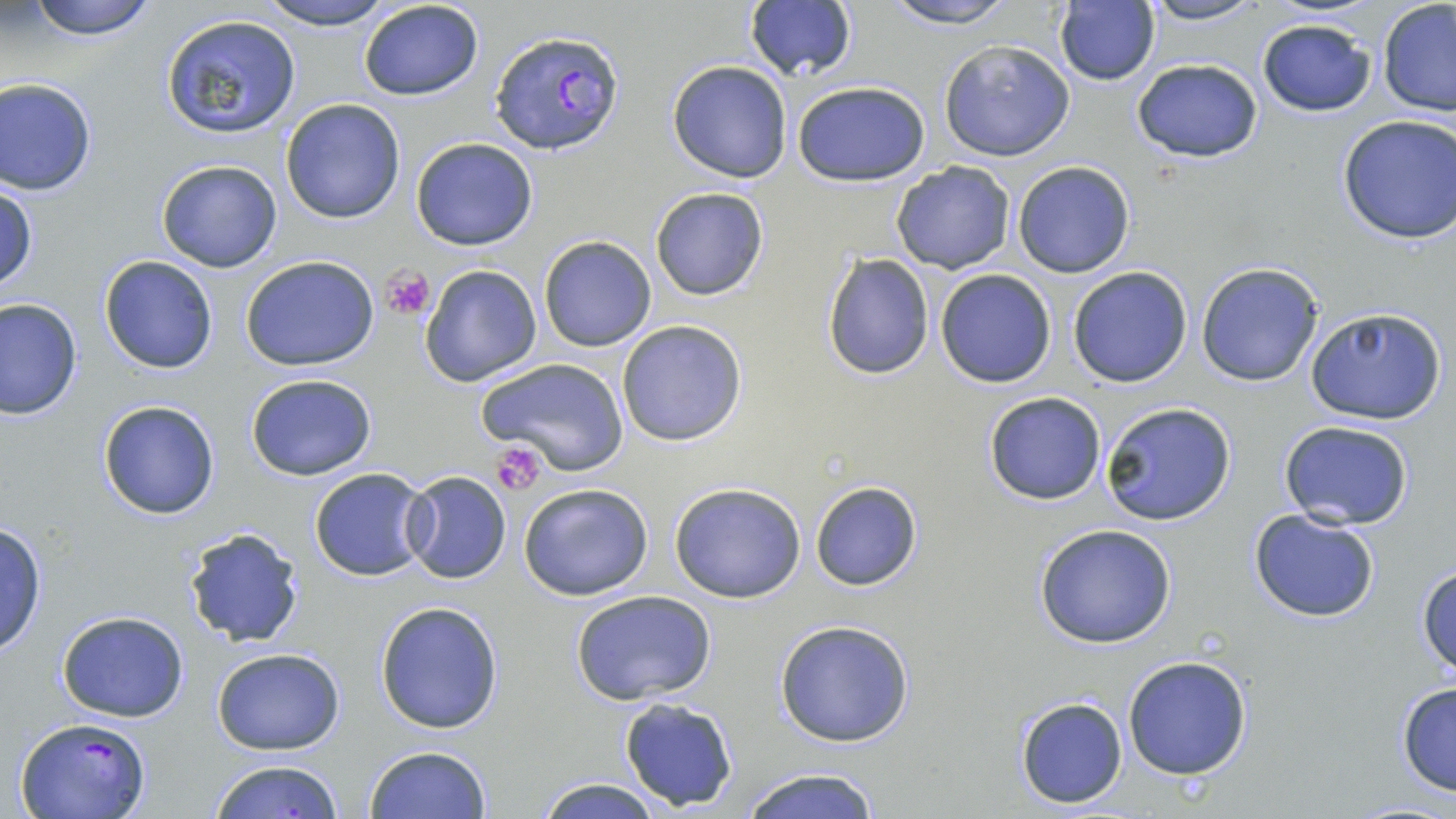
Summary:
  - Coordinate format: approximate bounding boxes as named x1/y1/x2/y2 corners in pixels
  - Platelet locations: (x1=378, y1=265, x2=433, y2=319), (x1=490, y1=443, x2=549, y2=495)
  - Uninfected red blood cell locations: (x1=22, y1=0, x2=162, y2=41), (x1=253, y1=0, x2=400, y2=28), (x1=879, y1=0, x2=1023, y2=28), (x1=1140, y1=0, x2=1269, y2=26), (x1=357, y1=1, x2=484, y2=101), (x1=744, y1=1, x2=858, y2=83), (x1=1376, y1=2, x2=1456, y2=118), (x1=1054, y1=3, x2=1161, y2=85), (x1=160, y1=14, x2=303, y2=139), (x1=1257, y1=18, x2=1377, y2=117), (x1=937, y1=40, x2=1074, y2=162), (x1=1131, y1=59, x2=1263, y2=163), (x1=666, y1=60, x2=794, y2=183), (x1=0, y1=77, x2=99, y2=196), (x1=791, y1=79, x2=930, y2=187), (x1=279, y1=99, x2=406, y2=223), (x1=1336, y1=115, x2=1456, y2=245), (x1=409, y1=136, x2=538, y2=251), (x1=156, y1=160, x2=283, y2=273), (x1=890, y1=161, x2=1015, y2=274), (x1=1011, y1=161, x2=1136, y2=278), (x1=1, y1=183, x2=37, y2=296), (x1=650, y1=186, x2=770, y2=302), (x1=538, y1=236, x2=656, y2=352), (x1=821, y1=252, x2=936, y2=381), (x1=240, y1=253, x2=380, y2=372), (x1=98, y1=255, x2=218, y2=374), (x1=1195, y1=261, x2=1326, y2=387), (x1=419, y1=264, x2=544, y2=389), (x1=1067, y1=266, x2=1194, y2=388), (x1=934, y1=269, x2=1057, y2=388), (x1=0, y1=299, x2=82, y2=421), (x1=1302, y1=307, x2=1447, y2=426), (x1=616, y1=320, x2=749, y2=447), (x1=479, y1=356, x2=631, y2=477), (x1=245, y1=372, x2=378, y2=482), (x1=982, y1=392, x2=1108, y2=507), (x1=96, y1=398, x2=221, y2=520), (x1=1099, y1=401, x2=1238, y2=526), (x1=1278, y1=421, x2=1417, y2=531), (x1=308, y1=467, x2=435, y2=581), (x1=401, y1=472, x2=512, y2=583), (x1=809, y1=480, x2=924, y2=591), (x1=518, y1=482, x2=655, y2=601), (x1=667, y1=482, x2=809, y2=603), (x1=1248, y1=507, x2=1382, y2=623), (x1=0, y1=521, x2=48, y2=659), (x1=1034, y1=525, x2=1177, y2=648), (x1=182, y1=526, x2=305, y2=647), (x1=1416, y1=561, x2=1456, y2=676), (x1=569, y1=589, x2=716, y2=706), (x1=375, y1=601, x2=504, y2=735), (x1=56, y1=609, x2=189, y2=723), (x1=772, y1=619, x2=917, y2=748), (x1=210, y1=647, x2=346, y2=755), (x1=1121, y1=654, x2=1253, y2=780), (x1=1395, y1=681, x2=1456, y2=797), (x1=1014, y1=695, x2=1127, y2=808), (x1=617, y1=697, x2=739, y2=809), (x1=364, y1=743, x2=493, y2=819), (x1=206, y1=759, x2=347, y2=819), (x1=733, y1=769, x2=885, y2=819), (x1=533, y1=776, x2=666, y2=819)
  - Plasmodium falciparum-infected red blood cell locations: (x1=490, y1=28, x2=625, y2=157), (x1=13, y1=715, x2=151, y2=819)
  - Slide-level diagnosis: Plasmodium falciparum
  - Image size: 1456×819 pixels
  - Magnification: 1000x
  - Modality: optical microscopy
  - Stain: May-Grünwald-Giemsa
  - Field of view: single
  - Preparation: thin blood smear